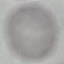

Malaria status: uninfected. Thin blood film. Cell patch, automatically extracted from a larger field of view and resized to 64 × 64 pixels. Giemsa-stained preparation. Photographed with a smartphone camera at the microscope eyepiece.